Describe the morphology of the erythrocytes.
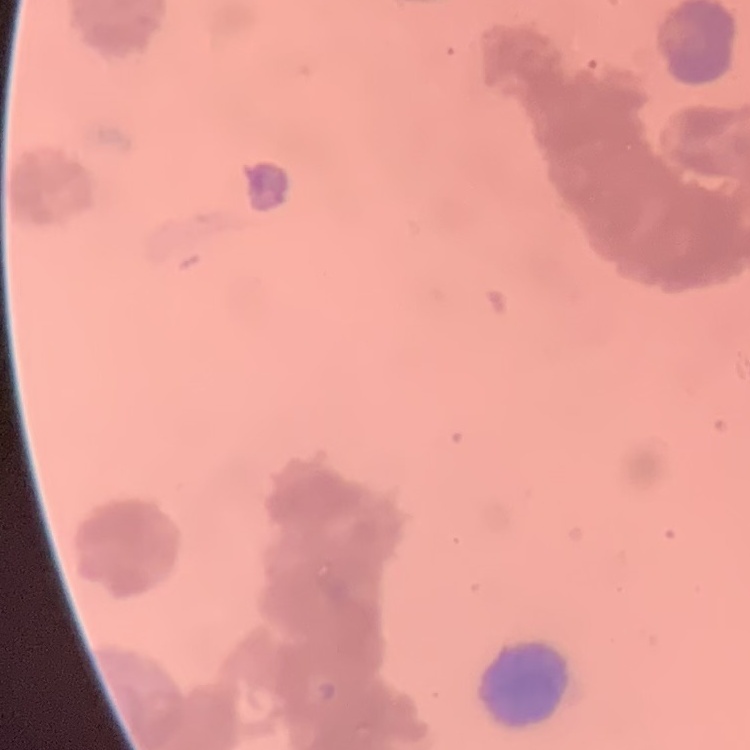
Rouleaux formation.

{
  "image_type": "one tile cut from a larger photomicrograph",
  "stain": "Field's or Giemsa",
  "preparation": "thin peripheral smear"
}